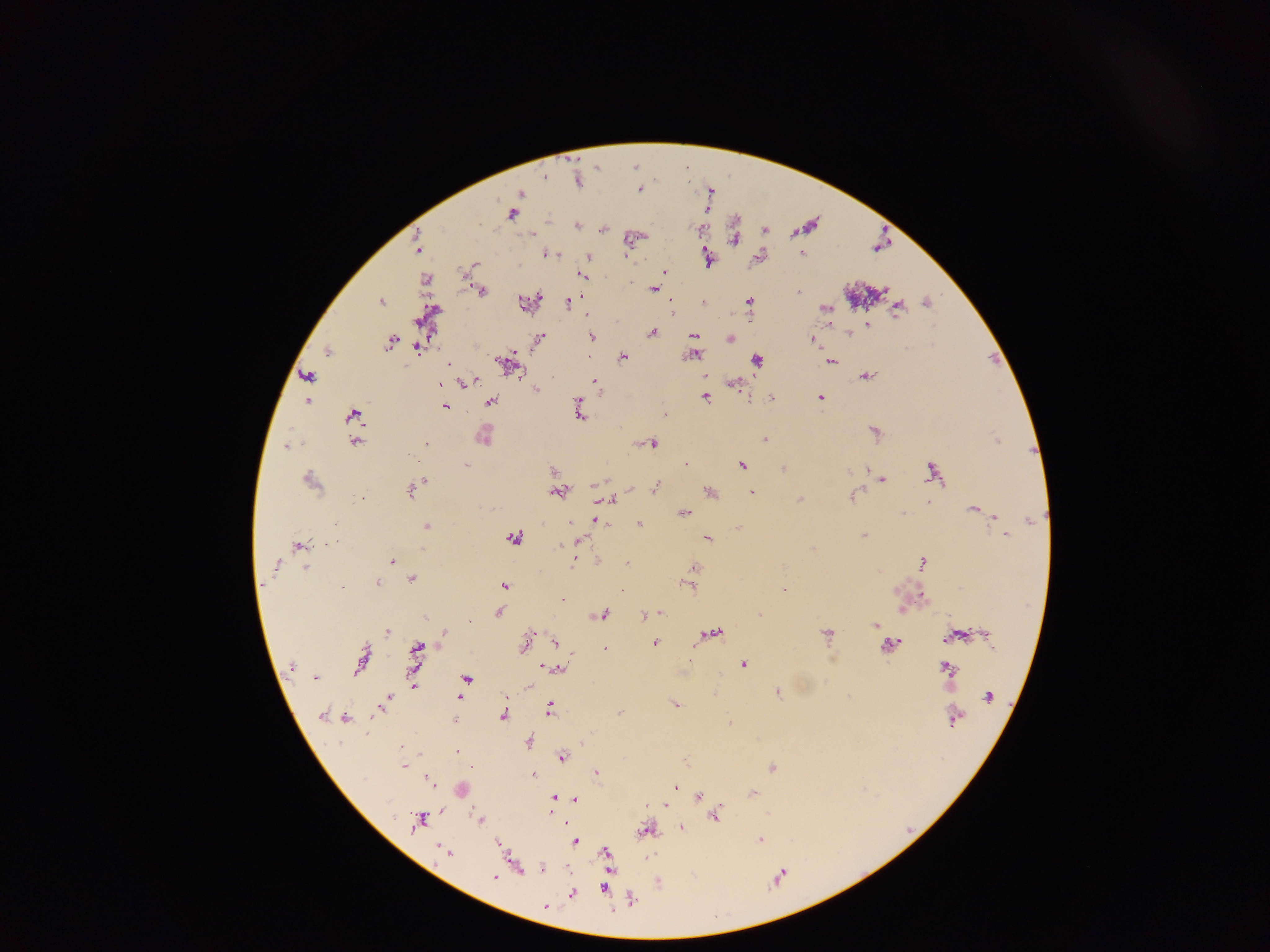
Approximate centers as {x, y} in pixels.
Summary:
  - Plasmodium parasite locations: {636, 165}, {598, 166}, {688, 167}, {546, 175}, {579, 180}, {640, 188}, {711, 189}, {521, 193}, {708, 209}, {514, 213}, {578, 225}, {808, 225}, {604, 228}, {765, 229}, {531, 233}, {636, 236}, {735, 236}, {420, 248}, {549, 253}, {558, 254}, {588, 258}, {759, 258}, {709, 260}, {473, 264}, {665, 271}, {583, 276}, {427, 277}, {655, 288}, {482, 290}, {800, 291}, {382, 300}, {750, 300}, {927, 300}, {530, 301}, {704, 302}, {568, 303}, {826, 308}, {898, 308}, {673, 309}, {430, 312}, {867, 324}, {653, 332}, {849, 333}, {592, 336}, {694, 337}, {730, 338}, {539, 339}, {391, 340}, {812, 340}, {420, 347}, {330, 350}, {694, 354}, {622, 356}, {993, 358}, {757, 359}, {510, 361}, {832, 361}, {448, 362}, {867, 375}, {309, 376}, {595, 381}, {466, 382}, {735, 383}, {441, 385}, {537, 388}, {706, 395}, {771, 397}, {821, 397}, {308, 400}, {491, 401}, {750, 401}, {445, 406}, {580, 412}, {665, 413}, {354, 414}, {875, 429}, {485, 437}, {766, 438}, {998, 439}, {356, 441}, {428, 442}, {653, 443}, {289, 444}, {467, 464}, {742, 464}, {784, 467}, {552, 468}, {933, 468}, {311, 476}, {882, 478}, {425, 480}, {656, 486}, {411, 490}, {560, 491}, {711, 491}, {752, 492}, {854, 495}, {363, 497}, {801, 498}, {610, 500}, {930, 501}, {975, 507}, {684, 512}, {596, 520}, {640, 523}, {427, 525}, {864, 534}, {1006, 534}, {515, 537}, {709, 538}, {578, 541}, {327, 542}, {300, 544}, {813, 548}, {575, 560}, {598, 560}, {392, 561}, {628, 561}, {924, 561}, {694, 567}, {307, 568}, {412, 577}, {378, 582}, {506, 584}, {690, 585}, {785, 588}, {922, 595}, {563, 598}, {501, 612}, {603, 613}, {662, 613}, {760, 613}, {644, 615}, {876, 624}, {388, 630}, {445, 632}, {713, 632}, {529, 633}, {828, 633}, {555, 641}, {656, 642}, {892, 642}, {525, 644}, {418, 646}, {605, 648}, {571, 656}, {745, 664}, {543, 666}, {947, 666}, {560, 668}, {359, 669}, {467, 678}, {414, 683}, {778, 692}, {461, 696}, {386, 700}, {676, 703}, {550, 707}, {620, 712}, {504, 714}, {348, 718}, {730, 720}, {529, 740}, {581, 742}, {402, 747}, {458, 750}, {563, 756}, {405, 764}, {772, 766}, {596, 772}, {535, 774}, {430, 779}, {676, 786}, {463, 789}, {753, 792}, {699, 796}, {554, 798}, {575, 800}, {666, 805}, {441, 811}, {716, 815}, {481, 818}, {419, 819}, {567, 822}, {682, 826}, {647, 830}, {761, 839}, {576, 841}, {499, 843}, {605, 851}, {448, 852}, {518, 868}, {542, 868}, {495, 877}, {780, 877}, {659, 882}, {605, 888}, {572, 894}, {632, 899}, {546, 906}
  - Image size: 1270×952 pixels
  - Capture: mobile-phone photograph through a microscope
  - Preparation: thick blood smear
  - Field of view: single
  - Country: Ghana